Classify this cell by malaria status.
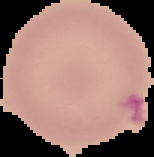
It is uninfected.

Summary:
  - Image size: 154×157 pixels
  - Image type: segmented cell region on a black background
  - Preparation: thin blood film